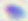

Summary:
  - Magnification: 400x
  - Identification: Toxoplasma gondii
  - Modality: photomicrograph